Name the parasite shown.
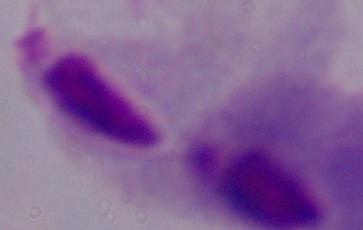
A trichomonad.

Summary:
  - Modality: micrograph
  - Magnification: 1000x